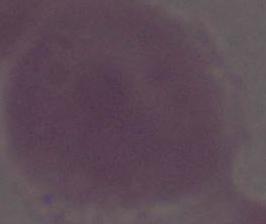
Summary:
  - Modality: micrograph
  - Identification: erythrocyte
  - Magnification: 1000x